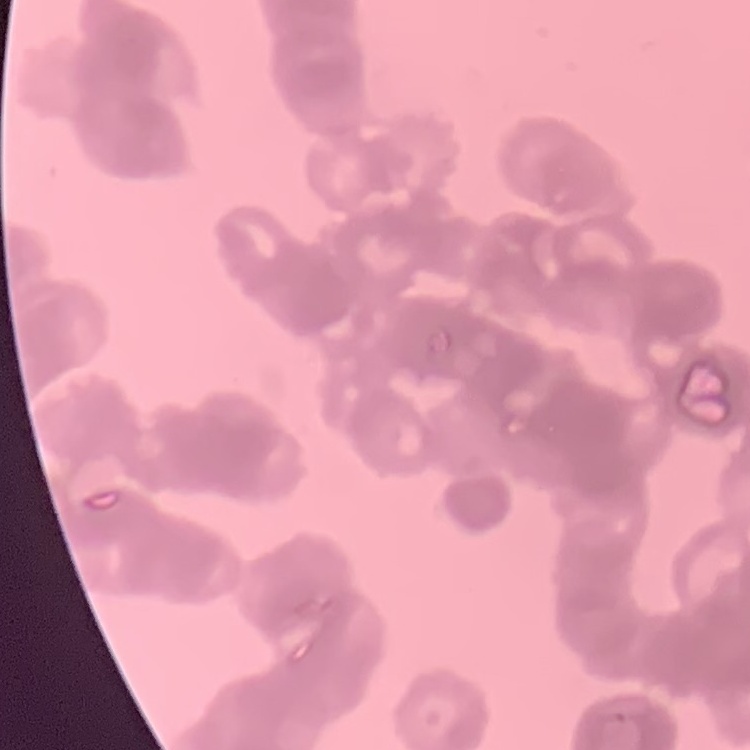
The erythrocytes exhibit rouleaux formation. Field's or Giemsa stain. Thin blood smear. Square crop of a larger photomicrograph.